Locate and identify every blood parasite.
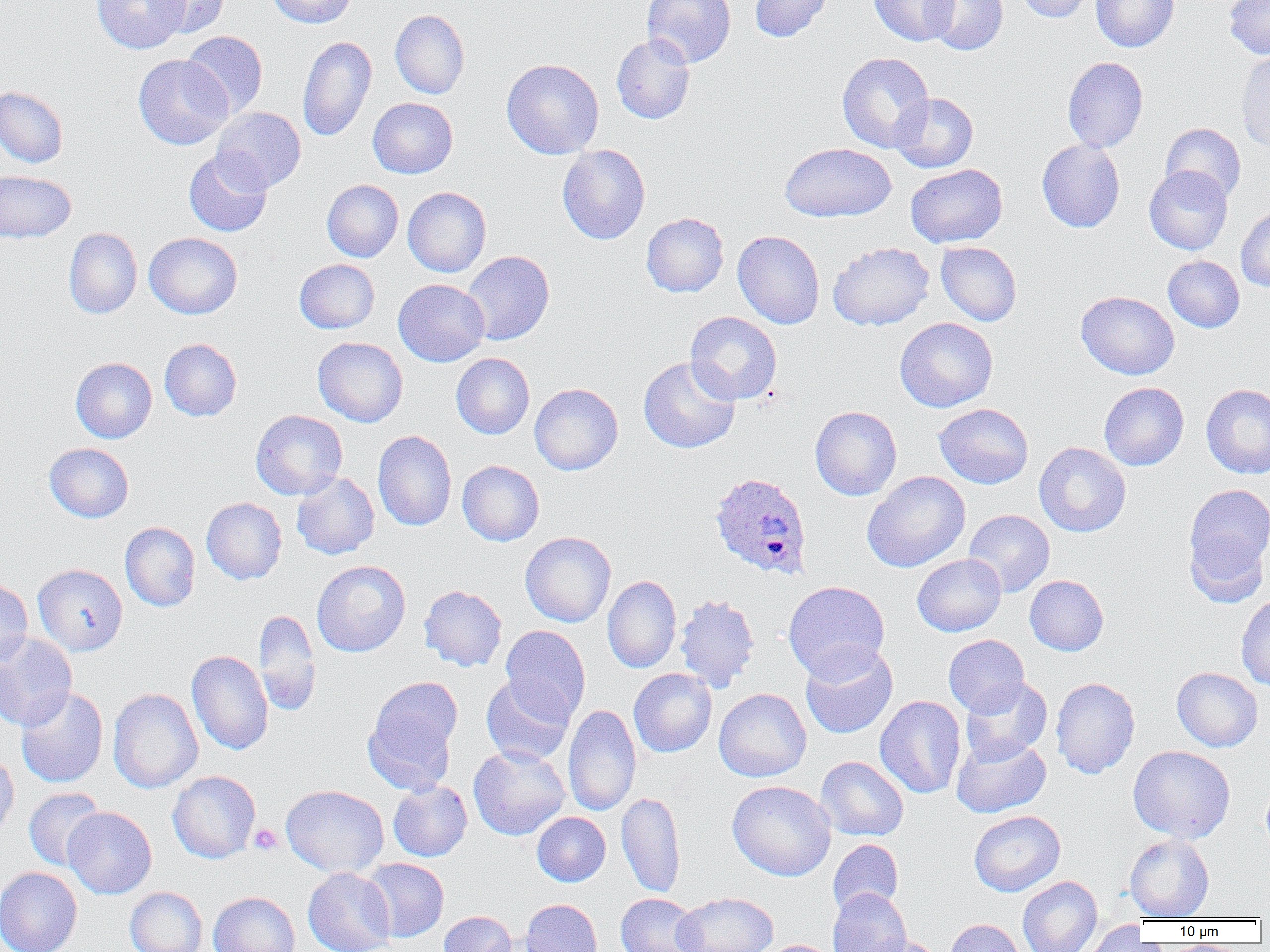
Approximate bounding boxes as (x1,y1)-(x2,y2) corner pairs in pixels.
Plasmodium ovale-infected red blood cells: (709,472)-(812,580).
No Plasmodium falciparum, Plasmodium malariae, Plasmodium vivax, Babesia divergens, or Trypanosoma brucei observed.

slide-level diagnosis = Plasmodium ovale
platelet locations = approximate bounding boxes as (x1,y1)-(x2,y2) corner pairs in pixels: (249,823)-(283,855)
uninfected red blood cell locations = approximate bounding boxes as (x1,y1)-(x2,y2) corner pairs in pixels: (91,0)-(188,54), (147,0)-(231,38), (266,0)-(356,28), (642,0)-(735,68), (749,0)-(834,42), (869,0)-(959,46), (923,0)-(1008,54), (1015,0)-(1097,23), (1091,0)-(1180,52), (1224,0)-(1270,59), (390,9)-(470,99), (181,31)-(268,118), (612,33)-(696,124), (297,36)-(376,142), (1236,50)-(1270,152), (837,52)-(934,152), (133,54)-(233,150), (1062,57)-(1148,152), (502,58)-(604,159), (0,86)-(68,167), (890,93)-(979,173), (367,97)-(458,178), (212,106)-(306,194), (1160,122)-(1246,203), (1036,139)-(1125,232), (780,143)-(897,222), (557,144)-(650,244), (184,150)-(272,236), (906,164)-(1007,248), (1144,165)-(1233,255), (0,170)-(76,243), (322,180)-(404,262), (403,187)-(491,277), (1235,205)-(1270,292), (641,212)-(728,297), (64,227)-(142,319), (733,230)-(825,329), (144,232)-(242,319), (935,241)-(1022,326), (828,242)-(934,330), (461,250)-(554,345), (1163,255)-(1244,332), (294,259)-(379,333), (393,279)-(489,366), (1076,291)-(1179,380), (685,312)-(782,404), (895,317)-(998,412), (313,336)-(408,427), (159,338)-(242,421), (451,353)-(535,439), (638,356)-(740,454), (71,357)-(157,443), (1099,382)-(1189,470), (529,383)-(623,475), (1201,383)-(1270,479), (933,403)-(1034,489), (810,406)-(902,500), (251,410)-(347,500), (373,430)-(457,531), (1034,442)-(1131,536), (44,443)-(134,522), (457,460)-(544,546), (862,471)-(970,573), (291,472)-(379,560), (1185,484)-(1270,577), (201,497)-(287,584), (964,510)-(1054,596), (120,522)-(201,612), (1185,530)-(1269,608), (520,532)-(616,627), (912,554)-(1006,636), (312,560)-(411,657), (33,563)-(127,655), (602,575)-(681,674), (1025,575)-(1109,655), (0,577)-(33,669), (783,580)-(890,682), (418,585)-(507,672), (1236,593)-(1270,692), (674,594)-(760,691), (253,609)-(321,716), (500,625)-(591,721), (0,632)-(77,731), (943,635)-(1030,716), (800,644)-(898,739), (187,650)-(273,756), (1171,667)-(1263,751), (628,669)-(717,757), (481,674)-(574,766), (363,676)-(462,793), (960,677)-(1052,764), (1050,677)-(1140,779), (16,687)-(108,788), (107,688)-(203,793), (714,688)-(811,782), (875,695)-(966,799), (563,704)-(641,816), (951,734)-(1051,818), (468,745)-(570,840), (1128,745)-(1235,843), (0,751)-(19,844), (815,756)-(909,841), (167,771)-(261,863), (1261,778)-(1270,856), (388,780)-(472,862), (726,780)-(836,881), (281,785)-(389,877), (23,788)-(106,871), (616,792)-(685,897), (63,807)-(157,899), (968,810)-(1065,897), (532,812)-(610,886), (1123,833)-(1214,921), (828,839)-(903,917), (360,858)-(448,942), (0,867)-(83,952), (303,867)-(397,952), (1018,875)-(1102,952), (125,887)-(207,952), (828,888)-(911,952), (209,892)-(300,952), (672,892)-(779,952), (616,893)-(704,952), (521,899)-(602,952), (439,911)-(517,952), (943,918)-(1027,952), (1075,921)-(1152,952), (859,936)-(943,952), (757,939)-(840,952)
field of view = single
image size = 1270×952 pixels
magnification = 1000x
modality = light microscopy
preparation = thin blood film